Point out each Plasmodium parasite.
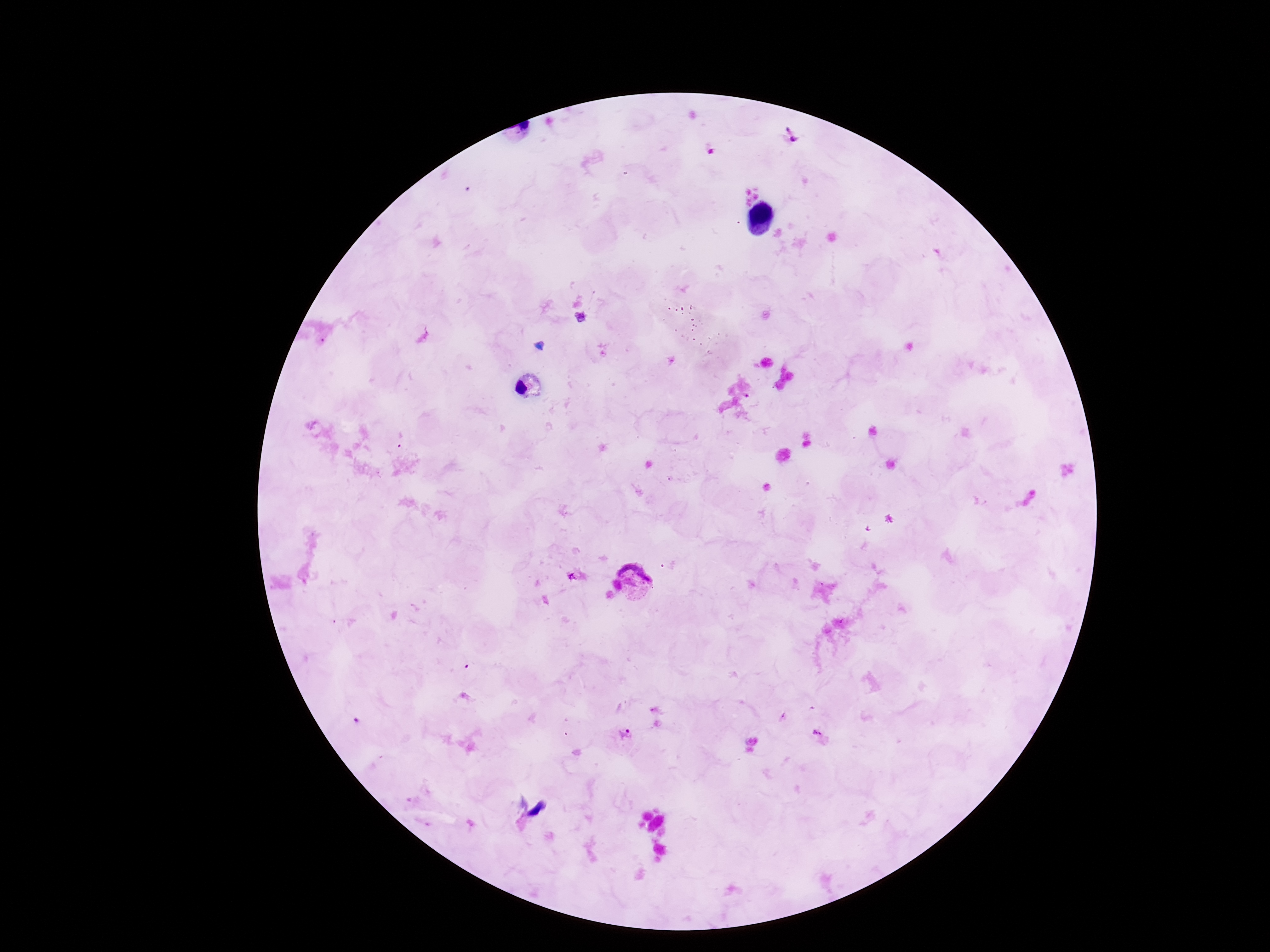
Approximate centers as {x, y} in pixels.
Plasmodium parasites: {789, 140}, {640, 580}, {626, 735}, {820, 736}.

Thick blood smear. Image is 1270×952 pixels. Giemsa stain. Photographed through the microscope eyepiece with a smartphone camera. Patient malaria status: positive. 100x magnification. Single field of view.